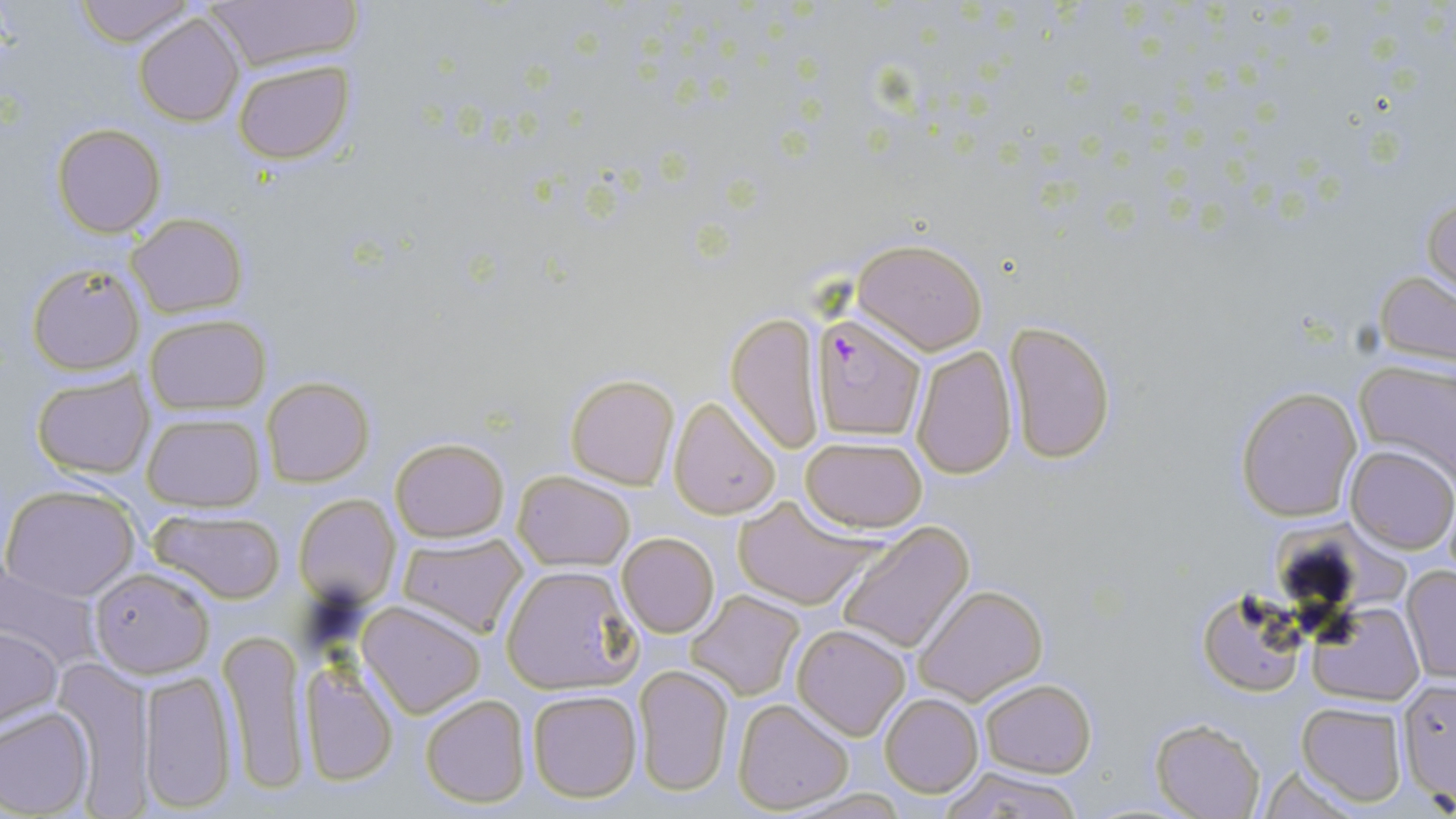 Approximate bounding boxes as (x1,y1)-(x2,y2) corner pairs in pixels. Uninfected red blood cell locations: (74,0)-(196,46), (201,0)-(361,69), (134,12)-(244,126), (233,60)-(352,164), (52,124)-(165,237), (1423,188)-(1455,301), (127,212)-(248,317), (852,239)-(988,354), (26,262)-(144,375), (1373,269)-(1456,370), (725,312)-(825,453), (144,314)-(270,415), (1003,319)-(1116,465), (911,344)-(1017,479), (1354,358)-(1456,485), (31,370)-(154,479), (564,373)-(680,489), (262,376)-(374,487), (1234,385)-(1363,523), (667,397)-(781,520), (141,411)-(265,512), (389,435)-(509,543), (800,436)-(928,531), (1346,445)-(1456,554), (513,469)-(635,570), (2,485)-(141,602), (293,494)-(401,609), (732,495)-(874,610), (147,505)-(286,604), (833,520)-(974,653), (396,532)-(530,639), (618,532)-(720,638), (2,563)-(105,675), (501,563)-(642,695), (1400,566)-(1456,684), (89,567)-(215,678), (912,583)-(1048,705), (687,590)-(805,702), (1199,590)-(1307,698), (358,600)-(487,718), (1309,600)-(1425,704), (792,624)-(911,741), (1,627)-(62,729), (218,628)-(309,794), (53,658)-(156,806), (296,662)-(399,786), (633,664)-(735,797), (138,668)-(237,812), (1396,678)-(1456,808), (979,679)-(1097,777), (526,689)-(642,804), (880,692)-(984,799), (420,694)-(532,809), (732,698)-(855,814), (1297,701)-(1408,807), (0,706)-(96,815), (1150,718)-(1266,818), (935,764)-(1085,819), (1251,765)-(1370,816). Plasmodium falciparum-infected red blood cell locations: (813,314)-(927,441). Slide-level diagnosis: Plasmodium falciparum. Image is 1456×819 pixels. Single field of view. May-Grünwald-Giemsa stain. 1000x magnification. Thin blood film. Optical microscopy.